Assess this cell for malaria.
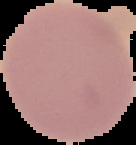

It is uninfected.

Cell region segmented out of the field of view; the surrounding area is masked to black. From a thin blood smear. Image is 136×145 pixels.